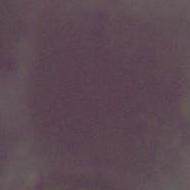
An erythrocyte is seen. 1000x magnification. Photomicrograph.